Describe the morphology of the erythrocytes.
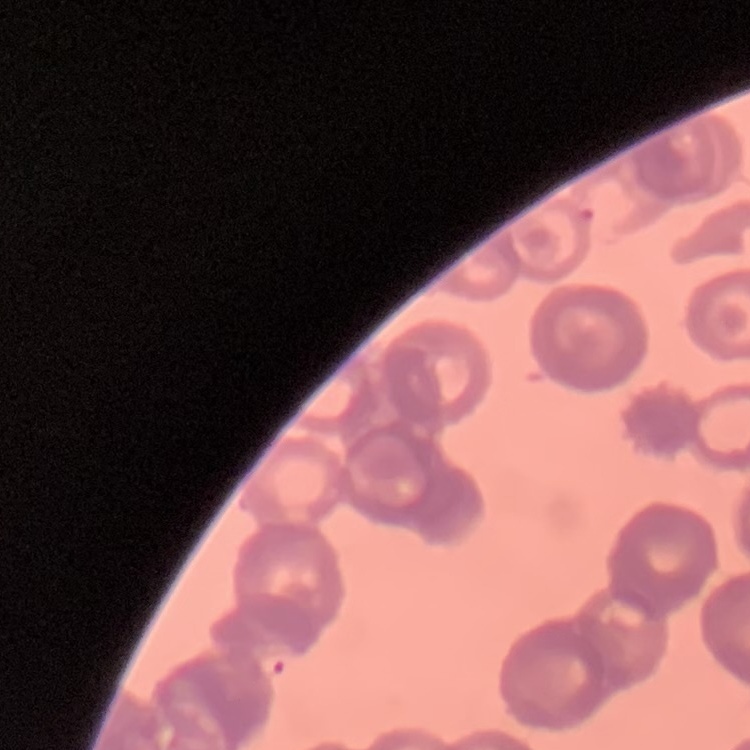

They show rouleaux formation.

Thin blood film. Stained with either Field's or Giemsa. Square crop of a larger photomicrograph.